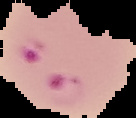

{
  "image_size": "136×118 pixels",
  "preparation": "thin blood smear",
  "result": "malaria parasites identified",
  "image_type": "segmented cell region on a black background"
}